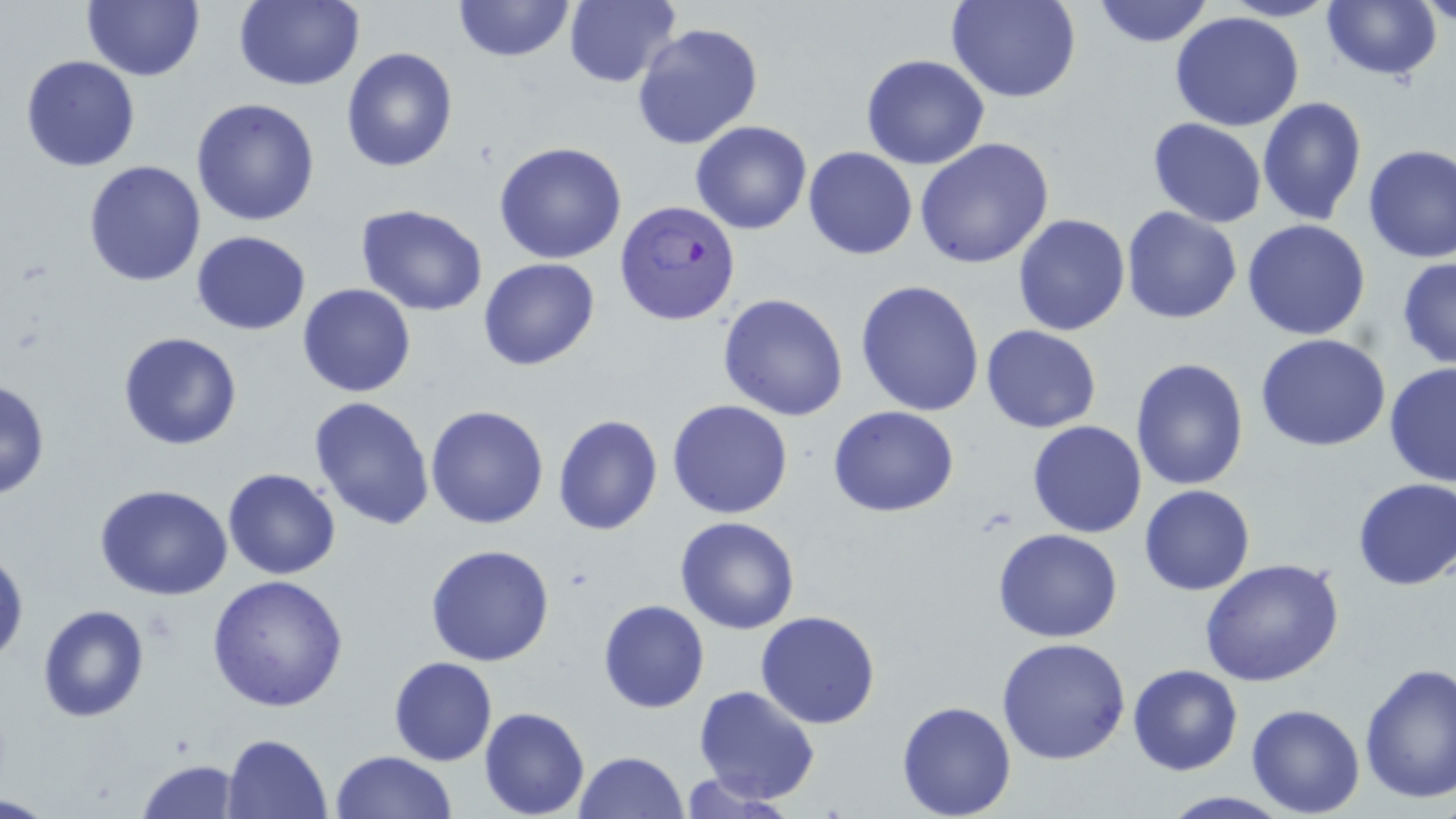
Approximate bounding boxes as named x1/y1/x2/y2 corners in pixels. Plasmodium falciparum-infected red blood cell locations: (x1=615, y1=198, x2=744, y2=327). Uninfected red blood cell locations: (x1=81, y1=0, x2=202, y2=82), (x1=234, y1=0, x2=366, y2=91), (x1=450, y1=0, x2=578, y2=64), (x1=565, y1=0, x2=681, y2=88), (x1=947, y1=0, x2=1079, y2=103), (x1=1090, y1=0, x2=1216, y2=49), (x1=1221, y1=0, x2=1339, y2=22), (x1=1420, y1=0, x2=1454, y2=30), (x1=1320, y1=1, x2=1441, y2=81), (x1=1170, y1=11, x2=1305, y2=131), (x1=631, y1=22, x2=764, y2=151), (x1=341, y1=46, x2=457, y2=174), (x1=21, y1=55, x2=140, y2=172), (x1=861, y1=55, x2=989, y2=171), (x1=1259, y1=96, x2=1368, y2=226), (x1=191, y1=97, x2=322, y2=227), (x1=1148, y1=118, x2=1267, y2=227), (x1=690, y1=120, x2=812, y2=235), (x1=915, y1=137, x2=1056, y2=269), (x1=495, y1=142, x2=627, y2=264), (x1=1361, y1=142, x2=1456, y2=265), (x1=802, y1=146, x2=918, y2=260), (x1=81, y1=159, x2=206, y2=287), (x1=355, y1=204, x2=489, y2=316), (x1=1121, y1=205, x2=1242, y2=324), (x1=1012, y1=213, x2=1130, y2=336), (x1=1242, y1=218, x2=1372, y2=340), (x1=190, y1=230, x2=312, y2=334), (x1=1396, y1=255, x2=1456, y2=369), (x1=478, y1=257, x2=600, y2=371), (x1=856, y1=279, x2=986, y2=417), (x1=298, y1=284, x2=417, y2=399), (x1=717, y1=292, x2=849, y2=422), (x1=981, y1=325, x2=1103, y2=434), (x1=117, y1=331, x2=243, y2=451), (x1=1256, y1=334, x2=1392, y2=453), (x1=1130, y1=358, x2=1250, y2=490), (x1=1384, y1=361, x2=1456, y2=487), (x1=0, y1=376, x2=49, y2=501), (x1=310, y1=395, x2=436, y2=530), (x1=667, y1=399, x2=795, y2=519), (x1=829, y1=404, x2=960, y2=516), (x1=425, y1=405, x2=550, y2=529), (x1=552, y1=414, x2=663, y2=536), (x1=1027, y1=420, x2=1146, y2=538), (x1=223, y1=468, x2=341, y2=581), (x1=1352, y1=476, x2=1456, y2=591), (x1=93, y1=483, x2=234, y2=600), (x1=1139, y1=485, x2=1256, y2=596), (x1=675, y1=517, x2=801, y2=634), (x1=993, y1=529, x2=1124, y2=642), (x1=425, y1=543, x2=555, y2=666), (x1=0, y1=547, x2=27, y2=667), (x1=1200, y1=559, x2=1345, y2=688), (x1=207, y1=574, x2=349, y2=710), (x1=597, y1=600, x2=709, y2=714), (x1=36, y1=604, x2=150, y2=723), (x1=755, y1=610, x2=883, y2=729), (x1=996, y1=637, x2=1131, y2=764), (x1=387, y1=655, x2=498, y2=766), (x1=1358, y1=662, x2=1456, y2=804), (x1=1127, y1=663, x2=1243, y2=776), (x1=693, y1=684, x2=820, y2=804), (x1=897, y1=701, x2=1017, y2=818), (x1=1245, y1=703, x2=1366, y2=817), (x1=479, y1=706, x2=590, y2=818), (x1=220, y1=732, x2=332, y2=818), (x1=328, y1=749, x2=458, y2=819), (x1=574, y1=750, x2=688, y2=818), (x1=135, y1=758, x2=241, y2=818), (x1=677, y1=774, x2=800, y2=817). Slide-level diagnosis: Plasmodium falciparum. Image is 1456×819 pixels. May-Grünwald-Giemsa stain. Thin blood film. Light microscopy. One field of a larger specimen. Captured at 1000x magnification.